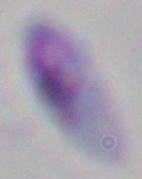
Toxoplasma gondii is seen. 1000x magnification. Micrograph.